Outline every parasitised red blood cell.
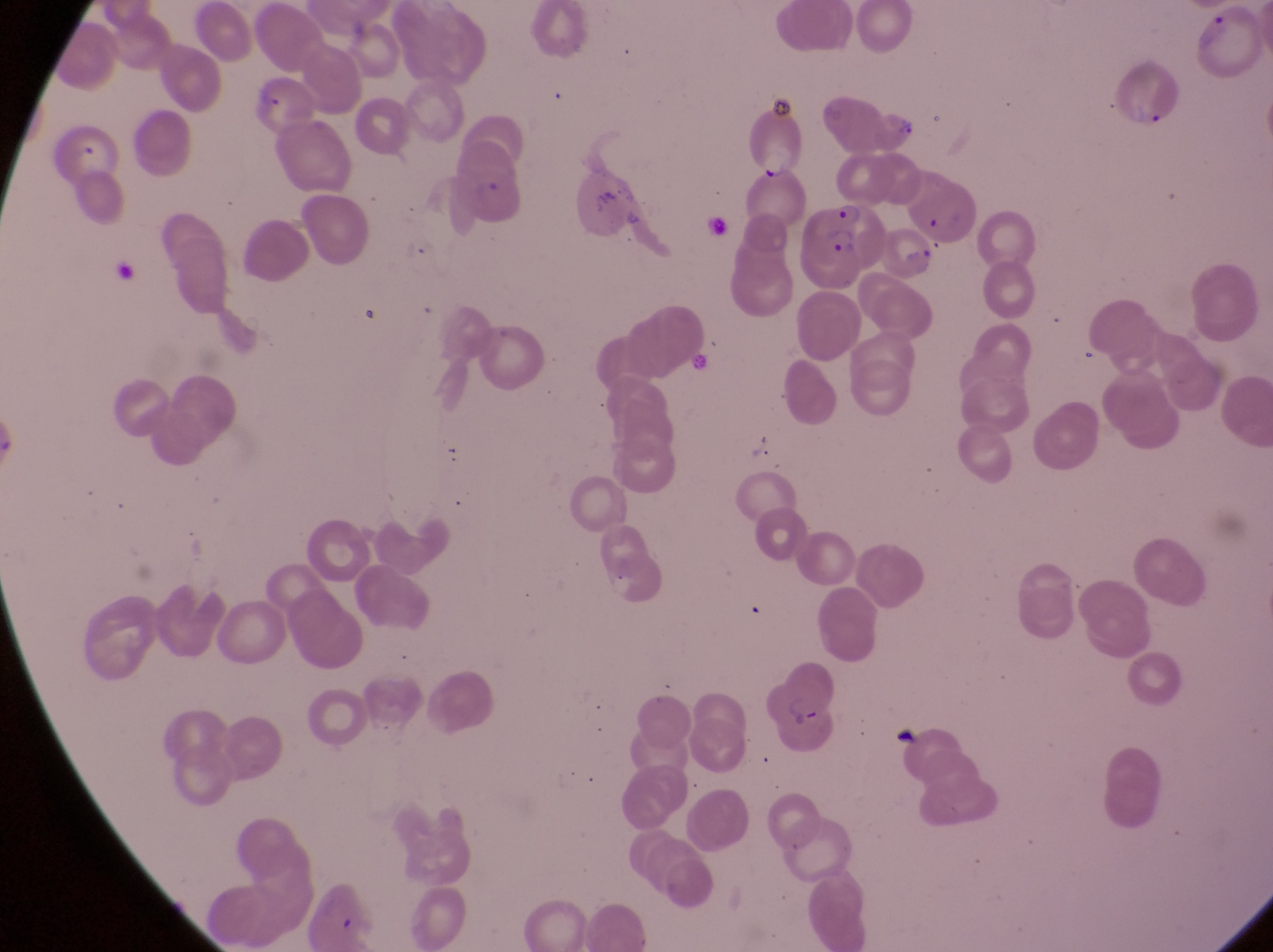
Approximate bounding boxes as (left, top, right, bottom) in pixels.
Parasitised red blood cells: (751, 112, 818, 182), (457, 160, 529, 230), (808, 197, 890, 285), (891, 222, 946, 280), (757, 662, 849, 744).

field of view = single
country = Uganda
image size = 1273×952 pixels
magnification = 1000x
capture = smartphone photograph through the eyepiece of an Olympus CX-23 microscope
artifact (platelet-like body, stain precipitate, or debris) locations = approximate bounding boxes as (left, top, right, bottom) in pixels: (63, 143, 98, 170), (586, 175, 621, 215), (702, 204, 747, 262)
preparation = thin blood film